Classify this cell by malaria status.
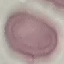
Uninfected.

Summary:
  - Stain: Giemsa
  - Capture: smartphone through the microscope eyepiece
  - Preparation: thin blood smear
  - Image type: cell patch, automatically extracted from a larger field of view and resized to 64 × 64 pixels